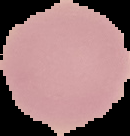
Summary:
  - Image type: segmented cell region with the area outside set to black
  - Image size: 130×136 pixels
  - Malaria status: uninfected
  - Preparation: thin blood film